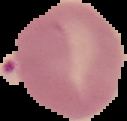

Summary:
  - Preparation: thin blood film
  - Image size: 127×121 pixels
  - Image type: segmented cell region with the area outside set to black
  - Result: Plasmodium parasites identified